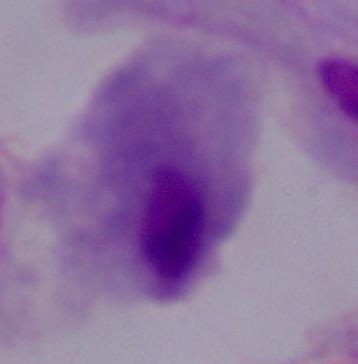 1000x magnification. A trichomonad is seen. Micrograph.